Identify the blood parasite species.
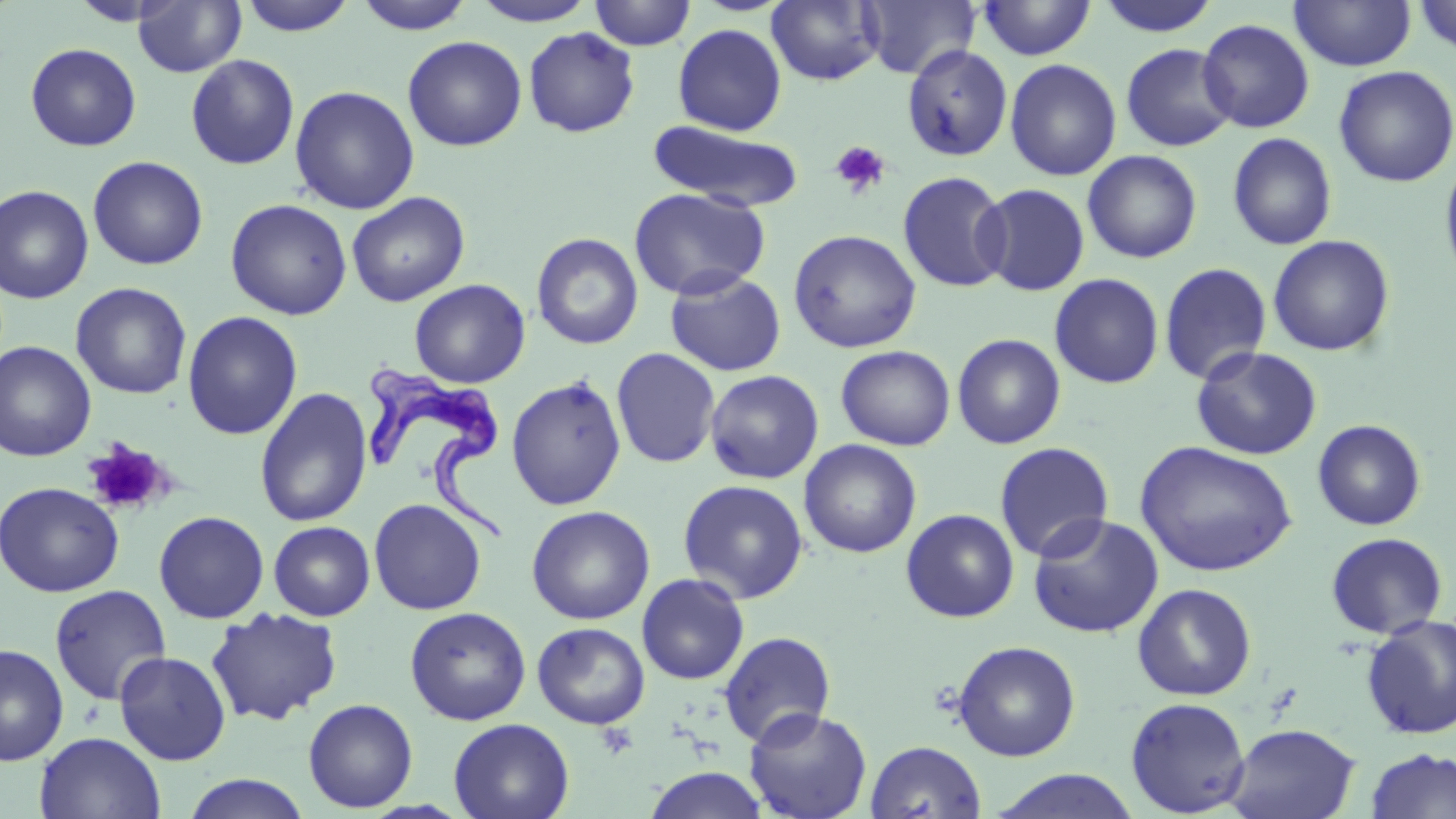
Trypanosoma brucei.

Summary:
  - Coordinate format: approximate bounding boxes as (x1, y1, x2, y2) in pixels
  - Trypanosoma brucei locations: (363, 356, 514, 544)
  - Uninfected red blood cell locations: (238, 0, 358, 36), (354, 0, 476, 34), (589, 0, 696, 50), (767, 0, 884, 86), (859, 0, 979, 80), (1095, 0, 1221, 38), (1290, 0, 1416, 72), (1413, 0, 1456, 59), (133, 1, 246, 77), (471, 1, 598, 26), (975, 1, 1097, 61), (1197, 18, 1315, 133), (672, 23, 788, 136), (523, 27, 641, 139), (402, 35, 527, 151), (25, 43, 142, 151), (1120, 43, 1237, 152), (902, 44, 1013, 162), (185, 54, 300, 170), (1004, 58, 1122, 181), (1333, 65, 1455, 188), (289, 85, 419, 214), (647, 120, 805, 212), (1227, 132, 1337, 250), (1083, 150, 1203, 263), (1439, 152, 1456, 290), (87, 155, 208, 270), (897, 170, 1012, 293), (976, 182, 1090, 296), (0, 185, 94, 304), (628, 187, 770, 300), (346, 191, 470, 307), (225, 198, 353, 320), (787, 228, 922, 353), (531, 232, 644, 350), (1267, 234, 1395, 356), (1159, 262, 1272, 386), (665, 269, 786, 377), (1049, 273, 1164, 389), (409, 278, 531, 388), (70, 282, 192, 399), (182, 310, 303, 440), (952, 333, 1066, 449), (0, 340, 97, 461), (835, 345, 956, 450), (1191, 345, 1322, 461), (611, 347, 721, 469), (704, 369, 824, 483), (506, 374, 627, 511), (254, 387, 374, 527), (1312, 419, 1427, 531), (798, 439, 922, 558), (1135, 440, 1297, 578), (994, 442, 1115, 562), (677, 478, 809, 604), (0, 481, 124, 597), (369, 498, 487, 615), (525, 505, 655, 625), (900, 508, 1019, 622), (153, 510, 269, 623), (1027, 513, 1164, 638), (268, 520, 375, 621), (1325, 532, 1449, 639), (636, 572, 750, 685), (1133, 583, 1257, 701), (49, 584, 172, 705), (404, 606, 531, 725), (205, 607, 343, 726), (1361, 614, 1456, 740), (532, 622, 651, 729), (718, 631, 836, 746), (952, 640, 1081, 761), (0, 644, 69, 767), (113, 650, 231, 766), (1125, 696, 1251, 816), (302, 698, 419, 812), (743, 706, 872, 819), (448, 718, 575, 819), (1224, 723, 1361, 819), (34, 731, 166, 818), (865, 740, 987, 819), (1364, 748, 1456, 819), (642, 766, 772, 819), (988, 769, 1143, 819), (180, 774, 313, 818)
  - Platelet locations: (828, 141, 891, 199), (82, 438, 173, 517)
  - Preparation: thin blood film
  - Image size: 1456×819 pixels
  - Modality: light microscopy
  - Magnification: 1000x
  - Stain: May-Grünwald-Giemsa
  - Field of view: one of a larger specimen